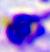
modality = micrograph
identification = white blood cell
magnification = 400x